Assess this cell for malaria.
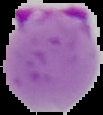

Parasitized.

From a thin blood film. The area outside the segmented cell region is set to black. Image is 103×115 pixels.